Report the malaria status of this cell.
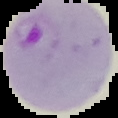

Parasitized.

Summary:
  - Image size: 118×118 pixels
  - Preparation: thin blood film
  - Image type: cell region segmented out of the field of view; surrounding area masked to black